Classify this cell by malaria status.
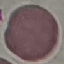

It is uninfected.

Summary:
  - Stain: Giemsa
  - Image type: cell patch, automatically extracted from a larger field of view and resized to 64 × 64 pixels
  - Capture: smartphone camera at the microscope eyepiece
  - Preparation: thin blood smear